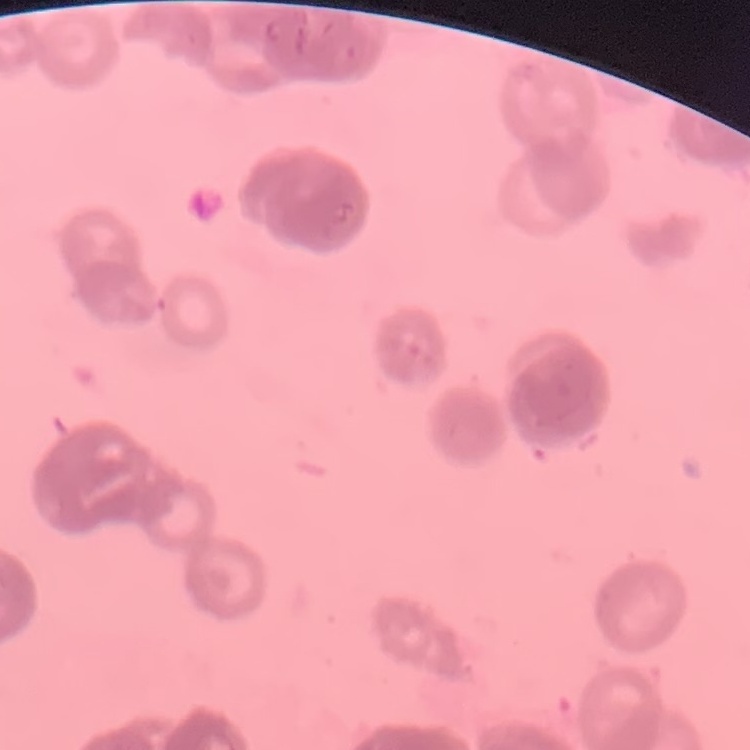

The red blood cells show rouleaux formation. Thin peripheral smear. One tile cut from a larger photomicrograph. Stained with either Field's or Giemsa.